Give the position of every leukocyte visible.
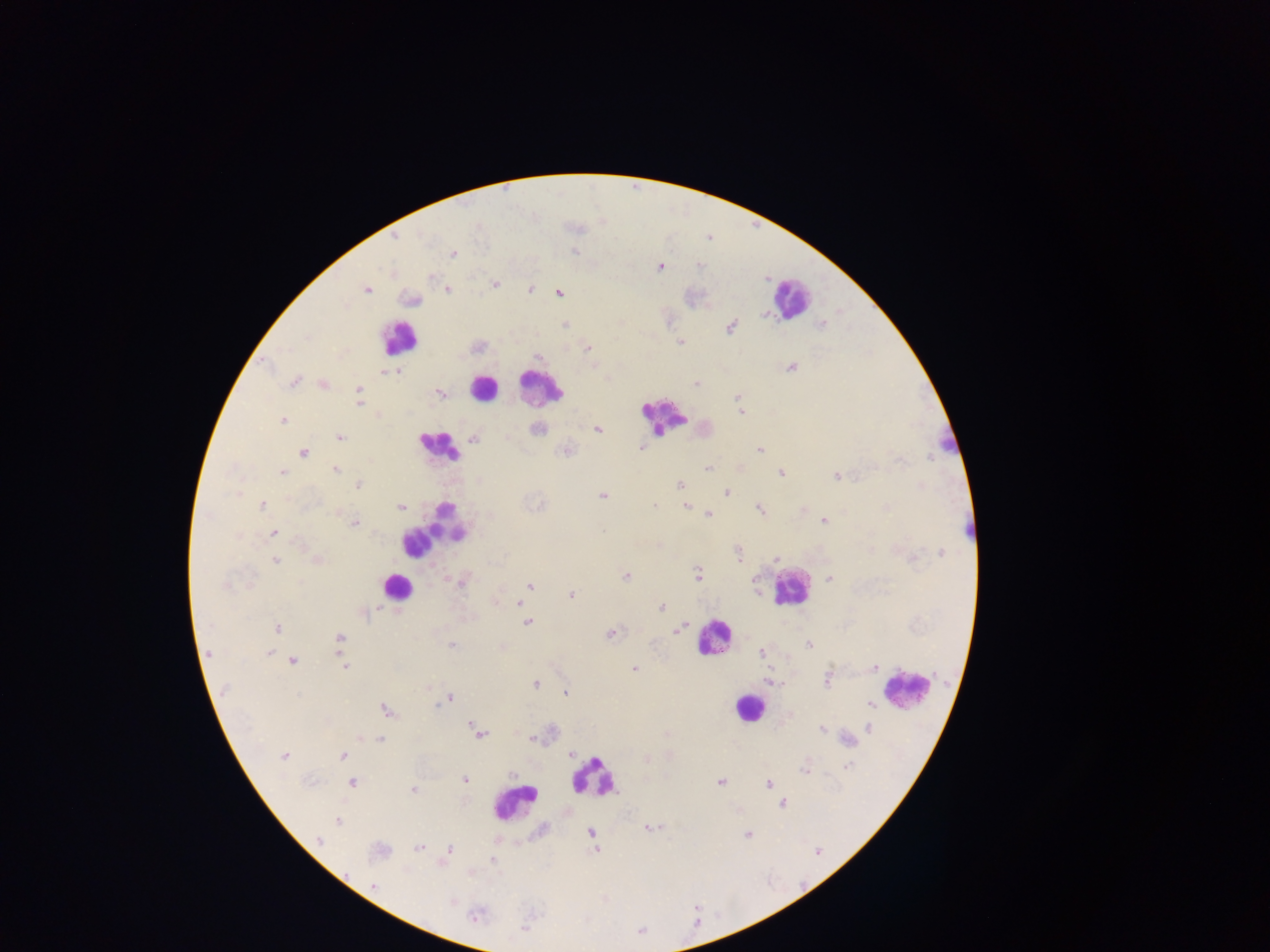

No leukocytes observed.

Approximate centers as (x, y) in pixels.
Summary:
  - Plasmodium parasite locations: (396, 240), (574, 250), (453, 253), (575, 254), (660, 267), (432, 276), (496, 283), (368, 289), (530, 289), (448, 290), (559, 294), (766, 314), (821, 323), (566, 326), (731, 328), (307, 337), (679, 343), (588, 348), (539, 358), (791, 369), (399, 372), (383, 373), (297, 377), (293, 382), (694, 384), (359, 390), (438, 392), (558, 395), (736, 399), (360, 403), (740, 412), (282, 420), (538, 429), (597, 429), (339, 438), (474, 439), (642, 447), (759, 449), (305, 453), (898, 458), (706, 469), (337, 471), (781, 472), (283, 473), (836, 476), (359, 484), (679, 484), (727, 492), (236, 494), (601, 497), (655, 504), (263, 505), (686, 506), (401, 507), (758, 509), (886, 509), (709, 514), (822, 519), (355, 523), (605, 531), (274, 534), (301, 542), (738, 553), (776, 559), (316, 560), (909, 560), (276, 561), (697, 575), (626, 577), (447, 578), (830, 579), (225, 584), (530, 584), (571, 595), (518, 603), (376, 606), (662, 609), (365, 614), (525, 618), (528, 623), (687, 624), (277, 628), (681, 629), (610, 635), (339, 638), (451, 645), (269, 652), (208, 653), (759, 653), (293, 660), (342, 660), (344, 666), (877, 669), (634, 670), (829, 677), (536, 683), (224, 690), (565, 692), (298, 694), (450, 697), (871, 704), (386, 710), (868, 727), (821, 728), (481, 735), (360, 737), (525, 738), (381, 741), (532, 741), (284, 755), (342, 756), (570, 757), (848, 764), (802, 772), (464, 780), (353, 783), (721, 784), (768, 784), (414, 790), (782, 804), (737, 809), (337, 820), (648, 829), (746, 836), (320, 839), (418, 848), (450, 848), (374, 888), (452, 903), (524, 929)
  - Image size: 1270×952 pixels
  - Capture: mobile-phone photograph through a microscope
  - Preparation: thick blood film
  - Country: Ghana
  - Field of view: single